Report the malaria status of this cell.
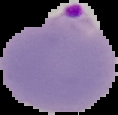
It is parasitized.

image type = segmented cell region with the area outside set to black
image size = 118×115 pixels
preparation = thin blood film